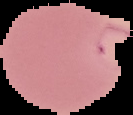 Malaria status: parasitized. The area outside the segmented cell region is set to black. From a thin blood smear. Image is 133×115 pixels.